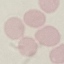

Summary:
  - Malaria status: uninfected
  - Preparation: thin smear
  - Stain: Giemsa
  - Image type: automatically extracted cell patch, resized to 64 × 64 pixels
  - Capture: smartphone through the microscope eyepiece